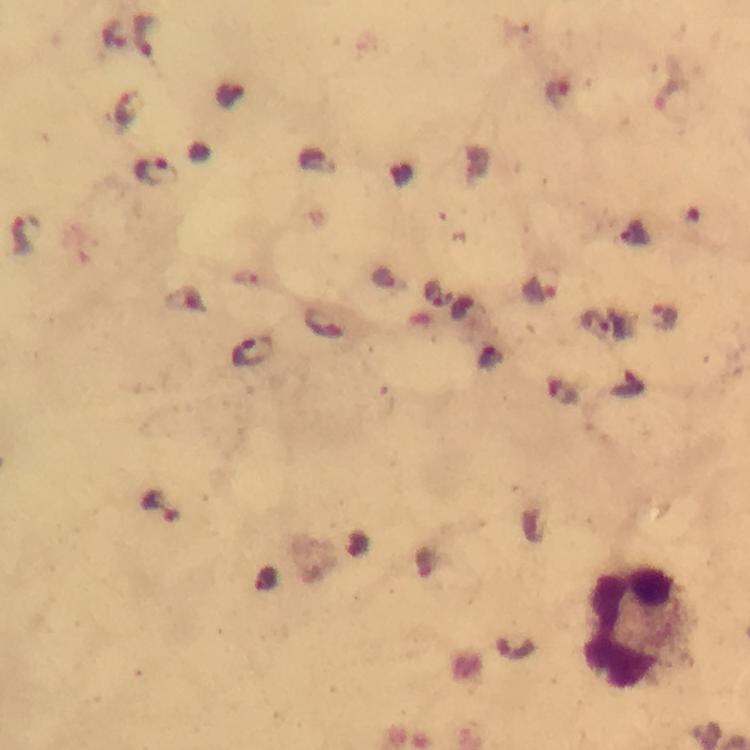
immersion oil = applied
image size = 750×750 pixels
malaria parasite locations = approximate centers as {x, y} in pixels: {114, 35}, {144, 36}, {128, 108}, {155, 171}, {24, 234}, {541, 290}, {665, 318}, {598, 324}, {252, 353}, {161, 504}
preparation = thick smear
stain = Giemsa
context = from a malaria diagnostic workup
magnification = 100x
cropped from = one field of view
capture = smartphone photograph through a microscope